State which parasite is depicted.
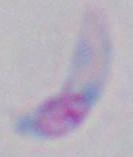

This is Toxoplasma gondii.

1000x magnification. Photomicrograph.